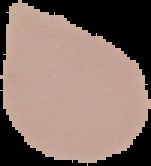
Summary:
  - Image size: 151×166 pixels
  - Malaria status: uninfected
  - Preparation: thin blood film
  - Image type: segmented cell region with the area outside set to black